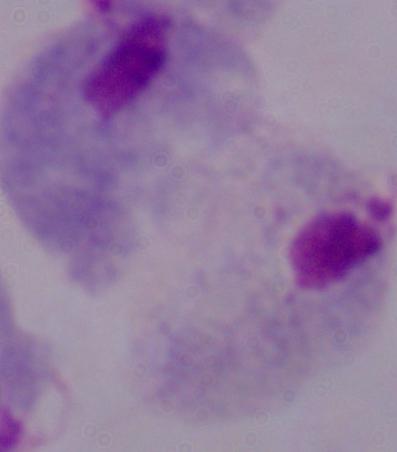 Micrograph. Captured at 1000x magnification. A trichomonad is seen.